Assess this cell for malaria.
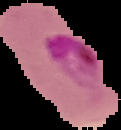

It is parasitized.

Summary:
  - Preparation: thin blood smear
  - Image size: 121×130 pixels
  - Image type: segmented cell region on a black background